Assess this cell for malaria.
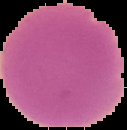
It is uninfected.

Image is 127×130 pixels. From a thin blood smear. The area outside the segmented cell region is set to black.